State the preparation type.
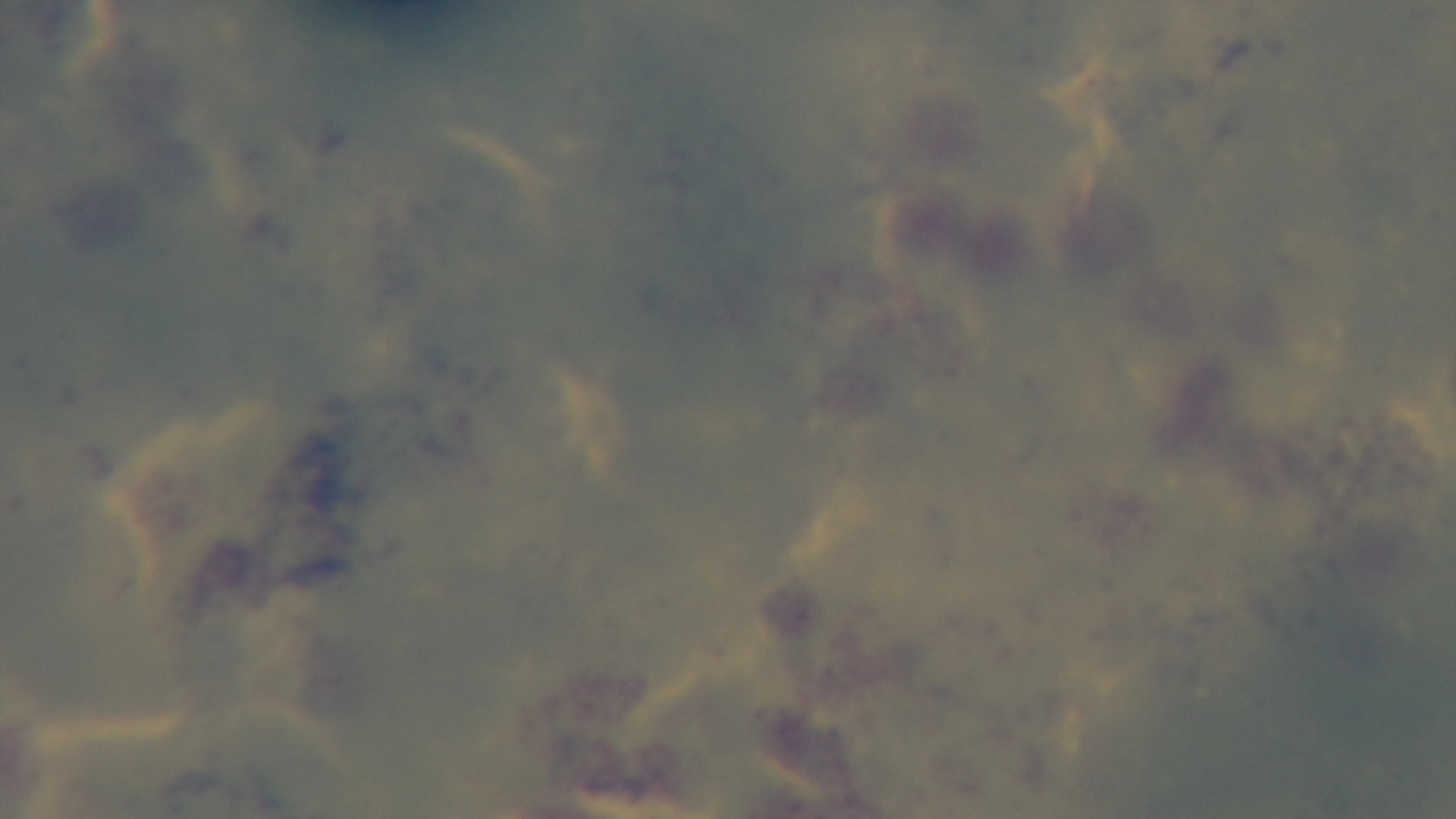
It is a thick blood film.

Summary:
  - Field of view: one from the slide
  - Capture: mounted 4K digital camera
  - Modality: light microscopy
  - Malaria status: uninfected
  - Objective: 100x oil immersion
  - Stain: Giemsa